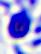
identification = leukocyte
magnification = 400x
modality = micrograph